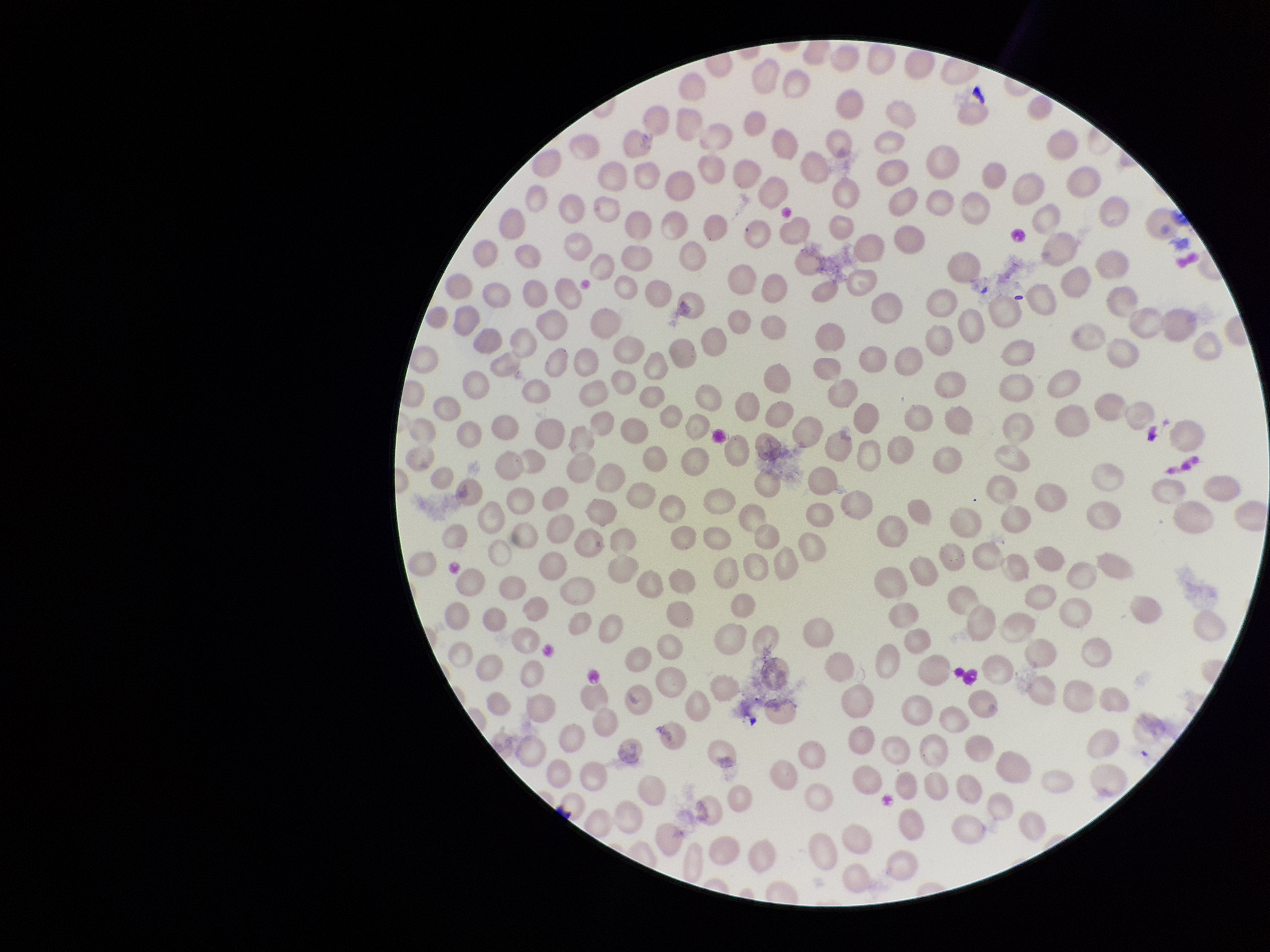

Parasitized red blood cells: none detected. Stained with Giemsa. Image is 1270×952 pixels. Preparation: thin blood smear. Patient malaria status: positive. Red blood cell count: 275. Species reported for this patient: Plasmodium falciparum. Single field of view. Parasitized red blood cell count: 0. Smartphone photograph taken through the eyepiece of a microscope.